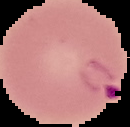

{
  "preparation": "thin blood film",
  "image_type": "cell region segmented out of the field of view; surrounding area masked to black",
  "image_size": "130×127 pixels",
  "result": "Plasmodium parasites detected"
}